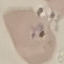
Result: malaria parasites identified. Cell patch, automatically extracted from a larger field of view and resized to 64 × 64 pixels. Photographed with a smartphone camera at the microscope eyepiece. Thin blood smear. Giemsa-stained preparation.